Outline each blood parasite and name the species.
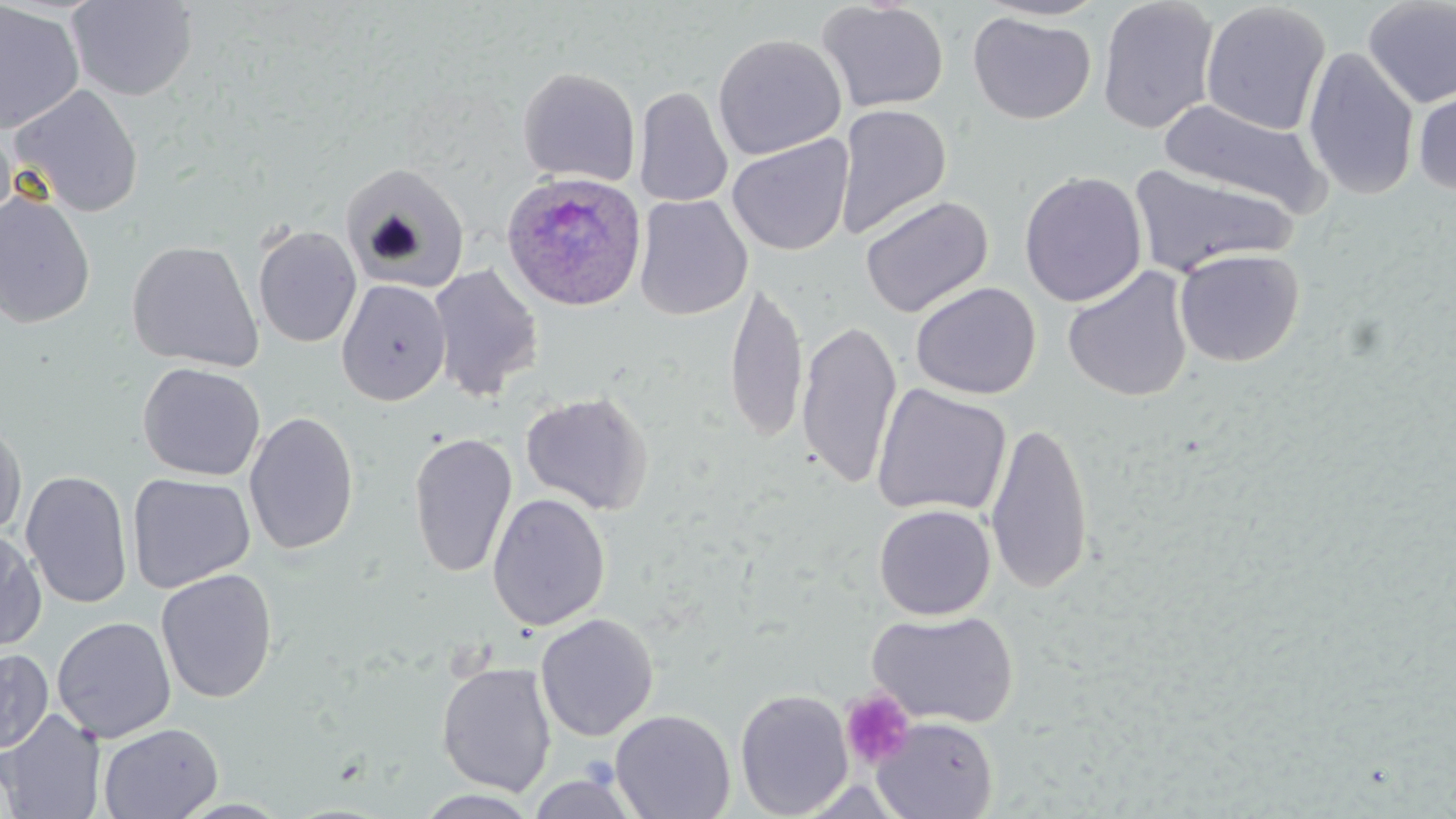

Approximate bounding boxes as (x1,y1)-(x2,y2) corner pairs in pixels.
Plasmodium ovale-infected red blood cells: (500,171)-(647,313).
No Plasmodium falciparum, Plasmodium malariae, Plasmodium vivax, Babesia divergens, or Trypanosoma brucei observed.

{
  "slide_level_diagnosis": "Plasmodium ovale",
  "uninfected_red_blood_cell_locations": "approximate bounding boxes as (x1,y1)-(x2,y2) corner pairs in pixels: (66,0)-(199,101), (974,0)-(1111,21), (1097,0)-(1220,135), (1361,0)-(1456,109), (816,1)-(949,114), (1,2)-(86,135), (1200,2)-(1332,136), (967,11)-(1097,125), (712,33)-(847,160), (1303,46)-(1420,201), (517,66)-(641,187), (1412,78)-(1456,201), (10,84)-(144,217), (633,85)-(733,209), (1159,97)-(1331,216), (834,104)-(952,238), (0,122)-(18,237), (727,134)-(854,256), (340,163)-(471,293), (1128,163)-(1297,277), (1019,171)-(1147,307), (0,190)-(96,328), (633,194)-(752,320), (859,195)-(994,318), (252,224)-(362,348), (126,240)-(264,372), (1173,248)-(1305,367), (427,263)-(544,402), (1062,265)-(1194,402), (336,279)-(451,406), (724,279)-(808,444), (910,281)-(1041,400), (796,319)-(903,489), (137,361)-(265,482), (871,383)-(1012,519), (520,391)-(653,515), (244,411)-(360,556), (0,416)-(27,540), (985,419)-(1094,595), (407,431)-(518,578), (20,470)-(134,610), (127,473)-(256,594), (487,493)-(611,631), (874,504)-(996,620), (0,527)-(47,651), (155,568)-(278,703), (866,608)-(1019,728), (535,613)-(659,741), (51,616)-(176,743), (0,648)-(53,754), (436,661)-(557,797), (735,688)-(854,818), (0,708)-(105,819), (610,709)-(735,819), (870,716)-(999,819), (98,722)-(223,819), (526,768)-(642,819), (414,789)-(543,818)",
  "platelet_locations": "approximate bounding boxes as (x1,y1)-(x2,y2) corner pairs in pixels: (840,690)-(916,771)",
  "stain": "May-Grünwald-Giemsa",
  "modality": "light microscopy",
  "magnification": "1000x",
  "field_of_view": "single",
  "image_size": "1456×819 pixels",
  "preparation": "thin blood smear"
}